Describe the morphology of the red blood cells.
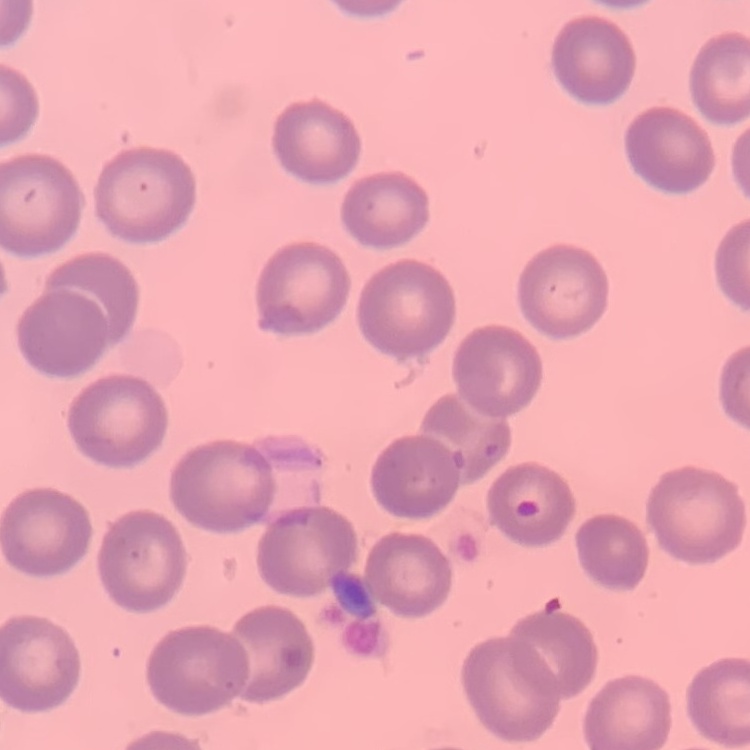

No rouleaux formation.

Stained with either Field's or Giemsa. One tile cut from a larger photomicrograph. Thin blood smear.